Name the cell type shown.
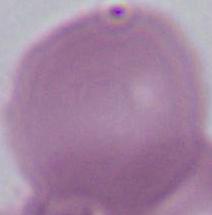

This is an erythrocyte.

Photomicrograph. 1000x magnification.